State which parasite is depicted.
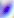
Toxoplasma gondii.

Summary:
  - Modality: photomicrograph
  - Magnification: 400x